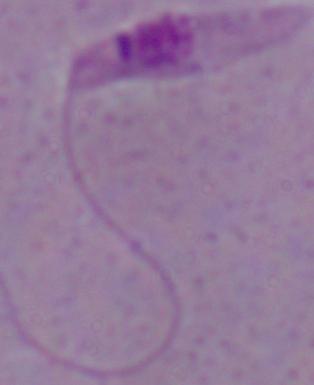

modality: micrograph
identification: Leishmania
magnification: 1000x